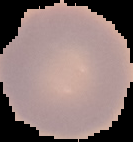

Summary:
  - Image type: segmented cell region with the area outside set to black
  - Result: negative for Plasmodium parasites
  - Image size: 133×142 pixels
  - Preparation: thin blood film